Name the blood parasite species.
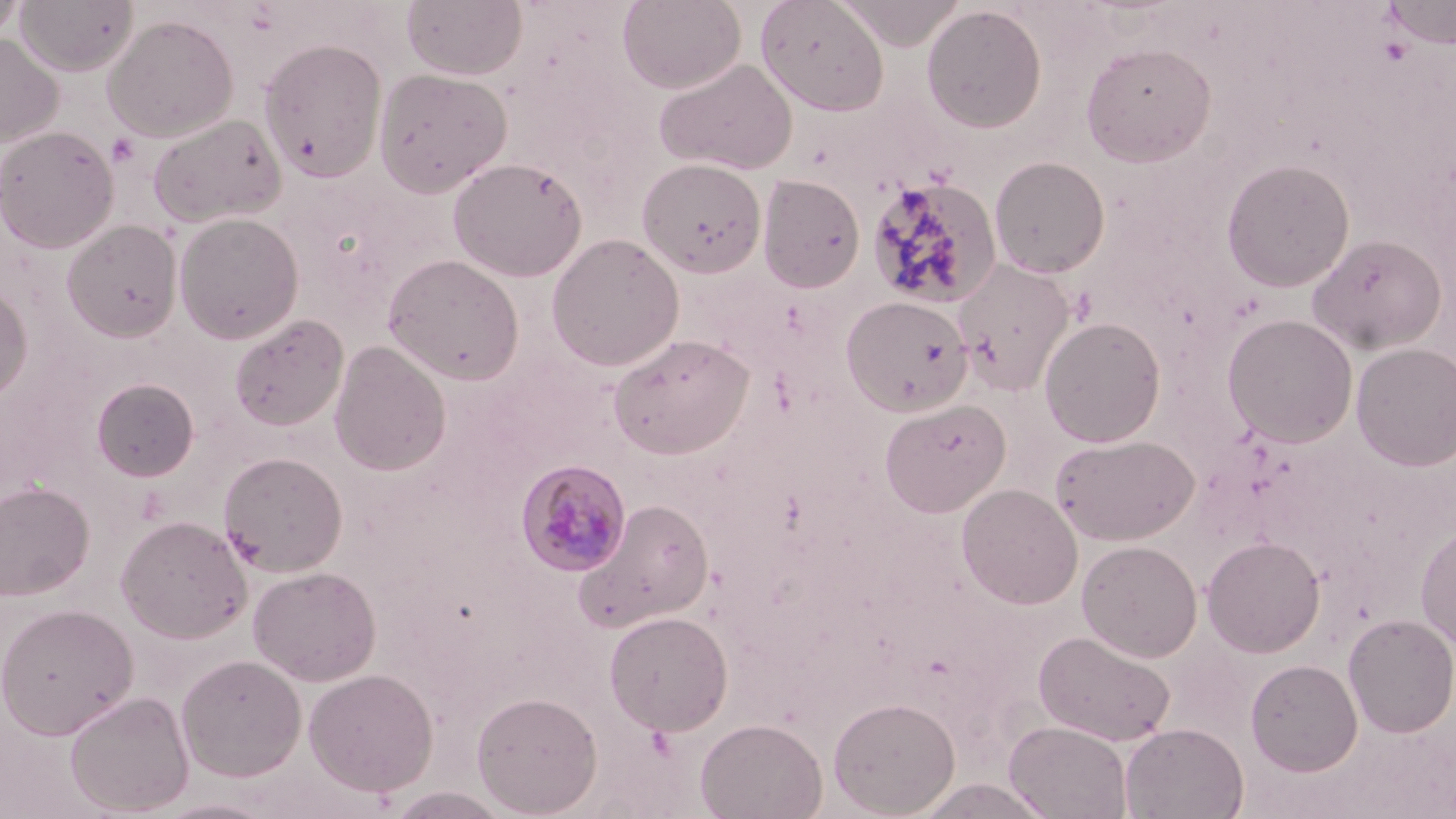

Plasmodium malariae.

Summary:
  - Coordinate format: approximate bounding boxes as named x1/y1/x2/y2 corners in pixels
  - Plasmodium malariae-infected red blood cell locations: (x1=514, y1=459, x2=632, y2=577)
  - Platelet locations: (x1=106, y1=133, x2=141, y2=168)
  - Uninfected red blood cell locations: (x1=15, y1=0, x2=139, y2=77), (x1=401, y1=0, x2=528, y2=82), (x1=617, y1=0, x2=746, y2=93), (x1=755, y1=0, x2=889, y2=115), (x1=835, y1=0, x2=964, y2=50), (x1=1383, y1=0, x2=1456, y2=47), (x1=0, y1=1, x2=27, y2=47), (x1=921, y1=5, x2=1048, y2=133), (x1=103, y1=14, x2=239, y2=143), (x1=0, y1=32, x2=63, y2=147), (x1=258, y1=38, x2=388, y2=182), (x1=1079, y1=41, x2=1217, y2=166), (x1=653, y1=57, x2=798, y2=175), (x1=373, y1=68, x2=512, y2=198), (x1=147, y1=111, x2=287, y2=228), (x1=0, y1=125, x2=119, y2=254), (x1=447, y1=156, x2=587, y2=282), (x1=989, y1=156, x2=1111, y2=278), (x1=636, y1=157, x2=767, y2=278), (x1=1221, y1=157, x2=1356, y2=292), (x1=757, y1=174, x2=865, y2=293), (x1=865, y1=176, x2=1002, y2=309), (x1=173, y1=212, x2=304, y2=344), (x1=61, y1=220, x2=182, y2=342), (x1=546, y1=233, x2=685, y2=372), (x1=1307, y1=233, x2=1446, y2=355), (x1=383, y1=253, x2=525, y2=386), (x1=952, y1=258, x2=1076, y2=395), (x1=0, y1=280, x2=33, y2=409), (x1=841, y1=295, x2=973, y2=416), (x1=229, y1=313, x2=349, y2=431), (x1=1222, y1=313, x2=1359, y2=447), (x1=1039, y1=316, x2=1167, y2=447), (x1=608, y1=333, x2=754, y2=459), (x1=329, y1=340, x2=451, y2=476), (x1=1351, y1=342, x2=1456, y2=472), (x1=91, y1=377, x2=200, y2=482), (x1=879, y1=398, x2=1011, y2=517), (x1=1052, y1=433, x2=1199, y2=544), (x1=219, y1=451, x2=348, y2=576), (x1=0, y1=480, x2=95, y2=601), (x1=956, y1=482, x2=1083, y2=609), (x1=575, y1=498, x2=715, y2=631), (x1=115, y1=515, x2=252, y2=643), (x1=1416, y1=521, x2=1456, y2=651), (x1=1202, y1=535, x2=1326, y2=657), (x1=1077, y1=539, x2=1203, y2=662), (x1=247, y1=565, x2=381, y2=686), (x1=0, y1=602, x2=138, y2=740), (x1=604, y1=610, x2=734, y2=735), (x1=1342, y1=613, x2=1456, y2=737), (x1=1033, y1=629, x2=1177, y2=746), (x1=176, y1=653, x2=307, y2=782), (x1=1245, y1=658, x2=1363, y2=776), (x1=304, y1=667, x2=439, y2=797), (x1=63, y1=689, x2=195, y2=816), (x1=471, y1=690, x2=603, y2=817), (x1=828, y1=696, x2=960, y2=818), (x1=695, y1=718, x2=827, y2=819), (x1=1004, y1=720, x2=1133, y2=819), (x1=1120, y1=723, x2=1249, y2=819), (x1=152, y1=797, x2=284, y2=819)
  - Preparation: thin blood film
  - Modality: optical microscopy
  - Stain: May-Grünwald-Giemsa
  - Field of view: one of a larger specimen
  - Magnification: 1000x
  - Image size: 1456×819 pixels